Assess this cell for malaria.
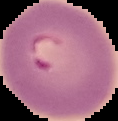

Parasitized.

Summary:
  - Preparation: thin blood film
  - Image size: 118×121 pixels
  - Image type: segmented cell region on a black background